Locate every malaria parasite by life-cycle stage, and every leukocyte.
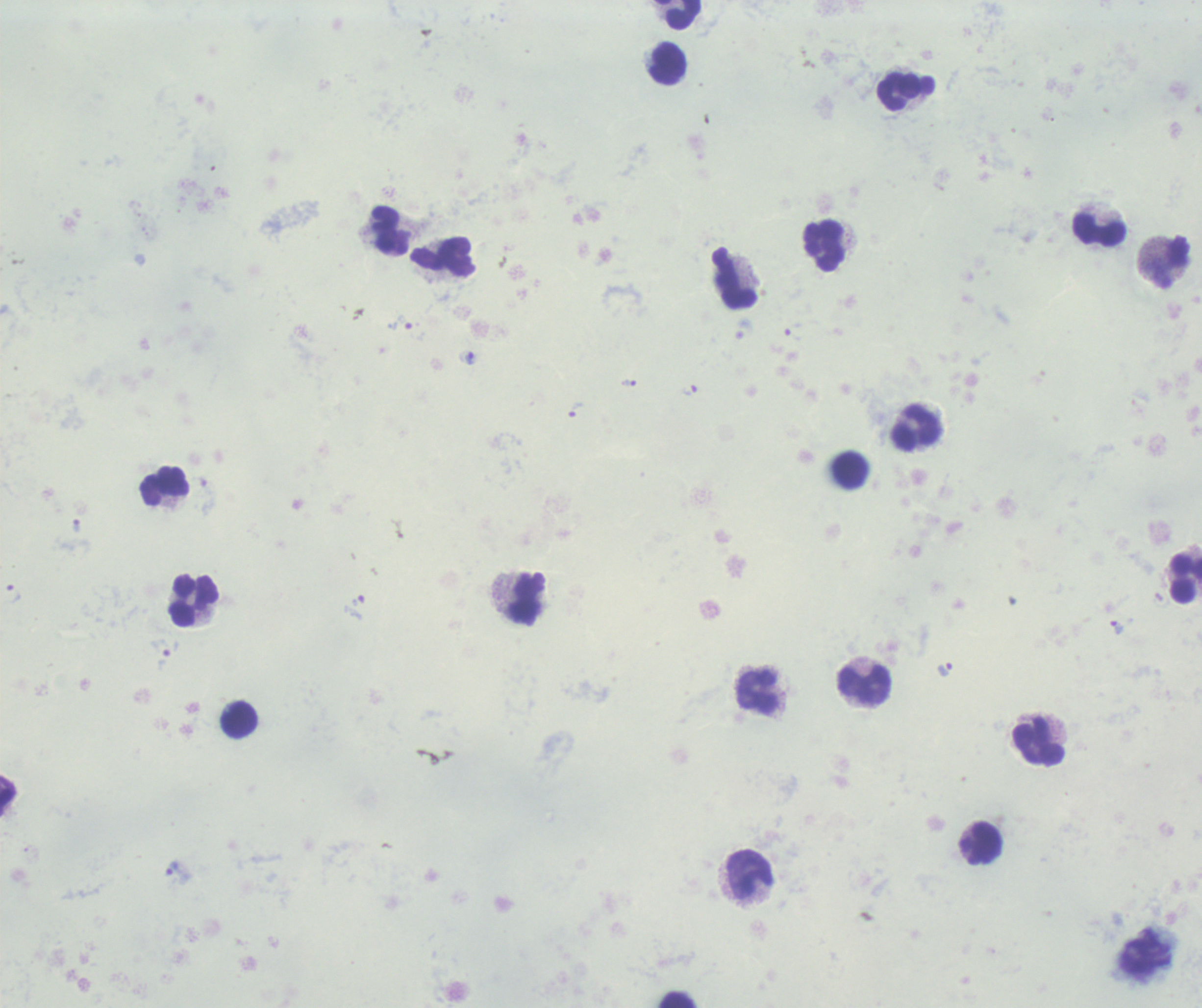

Approximate centers as [x, y] in pixels.
Trophozoites: [404, 323], [744, 329], [469, 358], [629, 383], [690, 391], [577, 410], [76, 526], [14, 594], [1116, 628], [165, 647], [945, 669], [177, 869].
No schizont or gametocyte forms observed.
Leukocytes: [679, 14], [669, 64], [906, 91], [1100, 230], [390, 231], [825, 246], [443, 258], [1173, 261], [734, 279], [917, 426], [850, 470], [165, 487], [1185, 577], [526, 599], [193, 602], [865, 686], [758, 693], [239, 720], [1039, 742], [985, 842], [749, 874], [677, 999].

Background quality: unsatisfactory. Thick blood film. One field from this slide. Previously used in a real diagnosis. 100x magnification. Image is 1202×1008 pixels. Romanowsky-stained preparation.